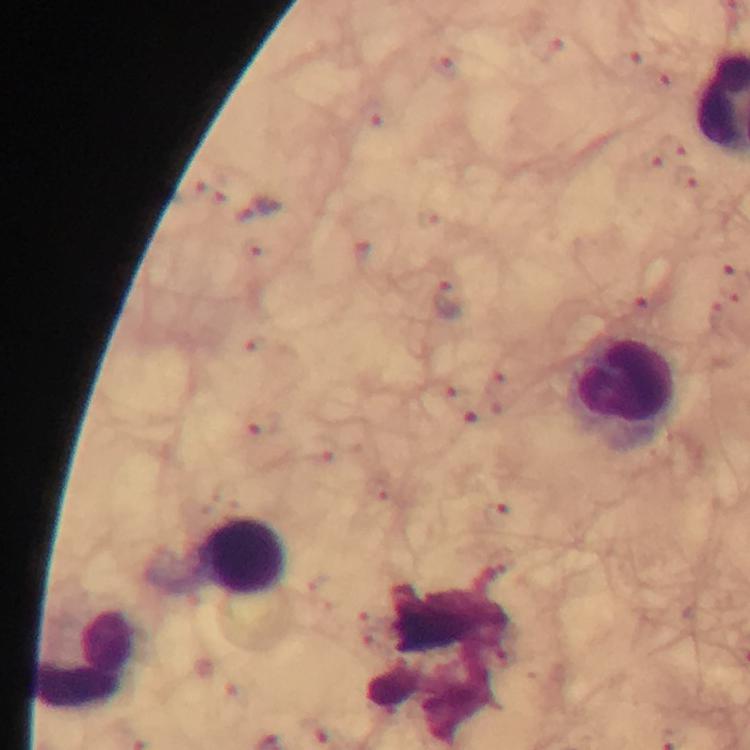

Approximate centers as (x, y) in pixels.
Summary:
  - Malaria parasite locations: (448, 300)
  - Leukocyte locations: (623, 388), (242, 557), (87, 658)
  - Immersion oil: used
  - Context: from a diagnostic examination for malaria
  - Cropped from: one field of view
  - Stain: Giemsa
  - Image size: 750×750 pixels
  - Preparation: thick blood film
  - Magnification: 100x
  - Capture: smartphone camera through the microscope